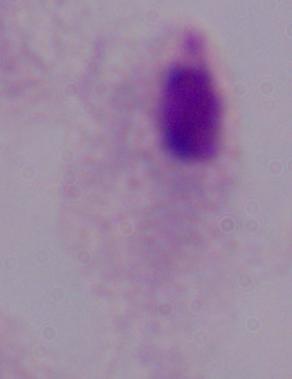

Photomicrograph. A trichomonad is shown. 1000x magnification.